Look for Plasmodium parasites.
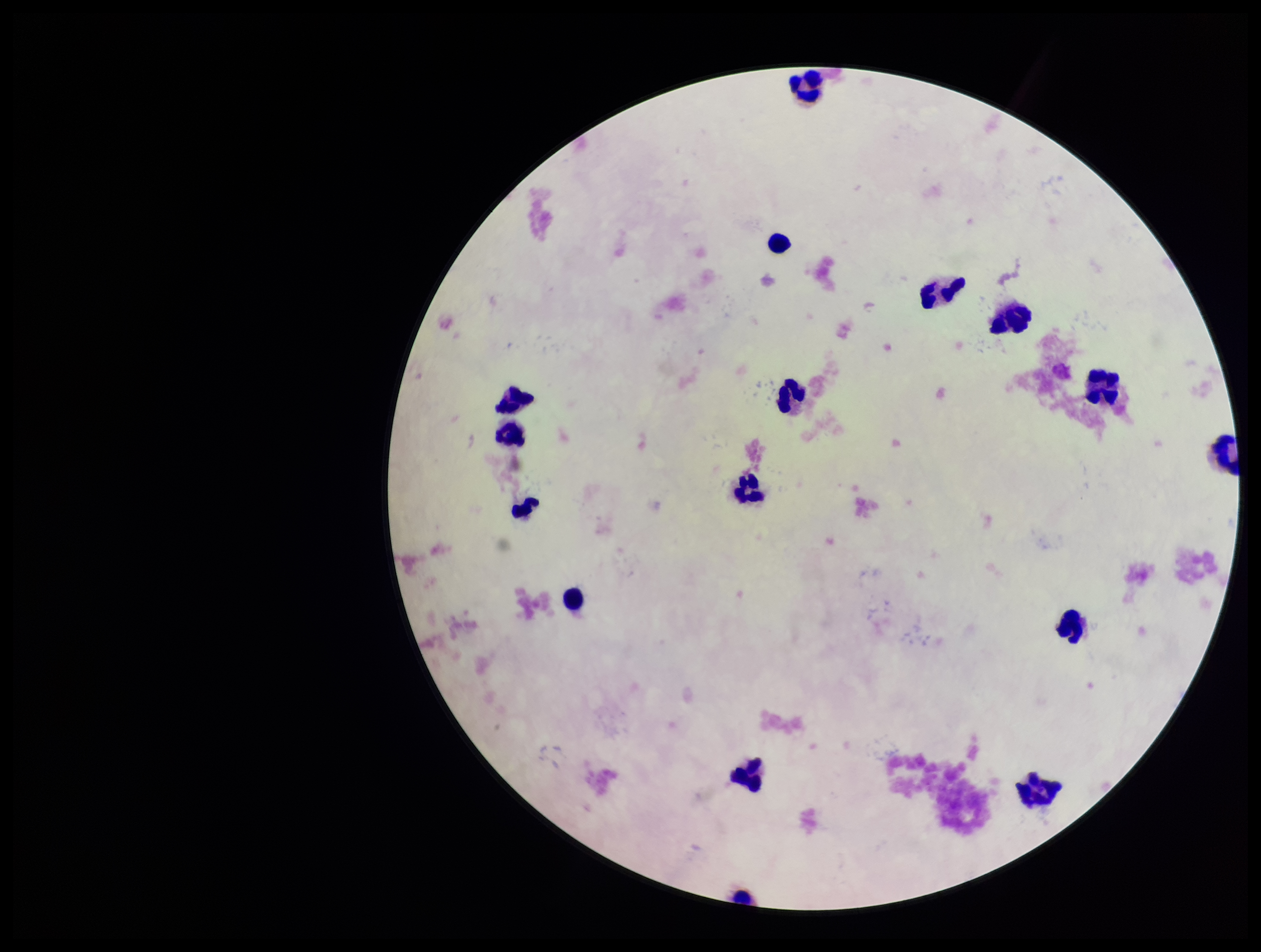
None detected.

Patient malaria status: negative. Single field of view. Leukocyte count: 16. Giemsa stain. Image is 1261×952 pixels. Photographed through the microscope eyepiece with a smartphone camera. Preparation: thick. Parasite count: 0.